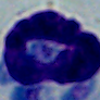

A white blood cell is shown. Photomicrograph. Captured at 1000x magnification.